Locate and identify every blood parasite.
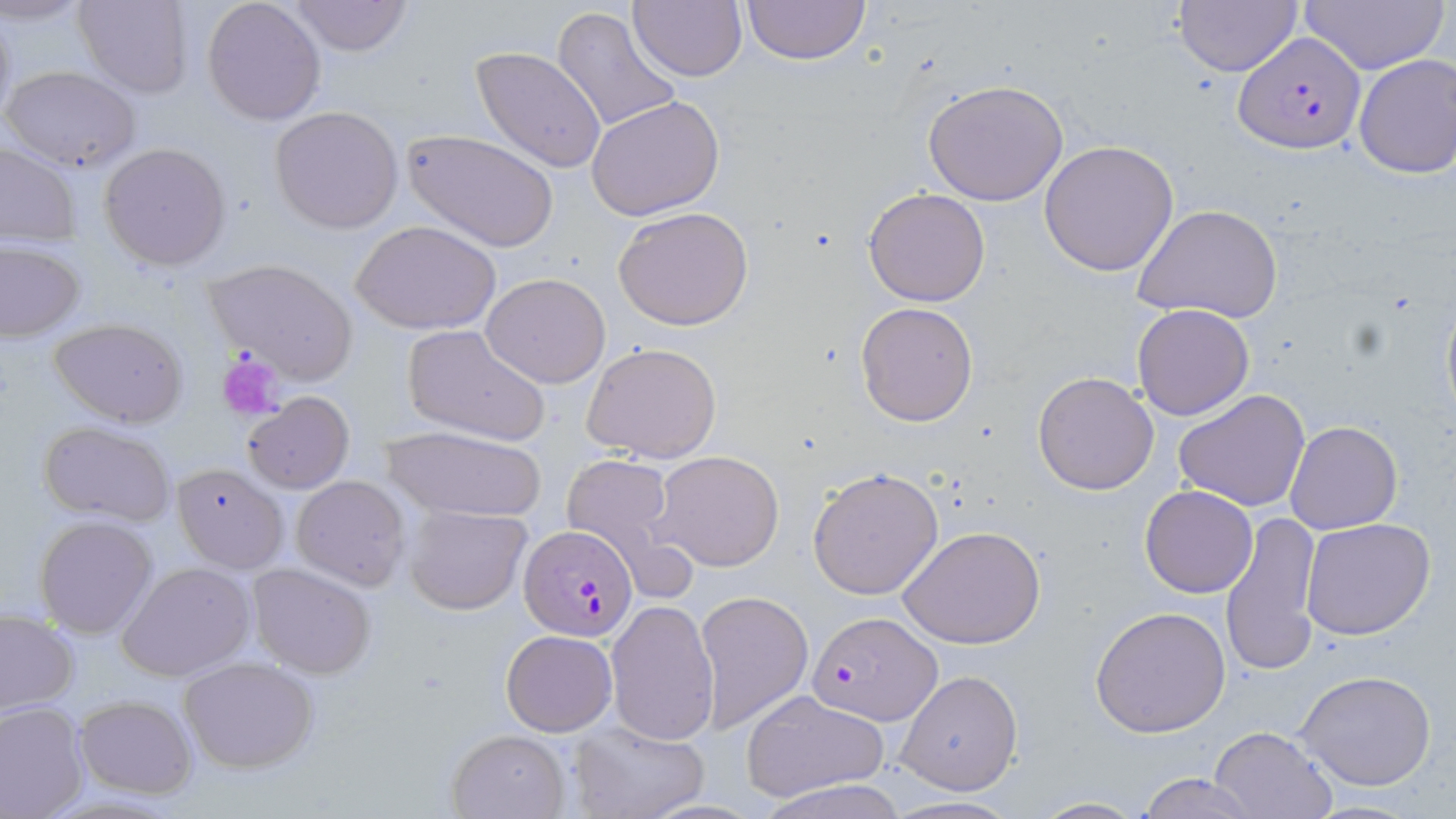

Approximate bounding boxes as [x1, y1, x2, y2] in pixels.
Plasmodium falciparum-infected red blood cells: [1234, 32, 1366, 155], [518, 524, 639, 641], [809, 611, 940, 726].
No Plasmodium ovale, Plasmodium malariae, Plasmodium vivax, Babesia divergens, or Trypanosoma brucei observed.

Summary:
  - Uninfected red blood cell locations: [73, 0, 192, 98], [201, 0, 327, 124], [289, 0, 414, 57], [628, 0, 746, 84], [741, 0, 873, 66], [1296, 0, 1448, 75], [1173, 1, 1303, 75], [0, 2, 18, 129], [551, 5, 683, 136], [471, 45, 607, 173], [1353, 53, 1456, 178], [1, 64, 143, 171], [924, 80, 1068, 208], [587, 95, 725, 221], [270, 106, 403, 232], [402, 127, 560, 254], [1039, 140, 1179, 276], [0, 141, 82, 248], [99, 142, 231, 270], [864, 187, 990, 307], [1136, 203, 1284, 326], [612, 206, 755, 332], [351, 219, 500, 335], [1, 241, 86, 340], [202, 258, 359, 383], [481, 274, 612, 389], [1440, 281, 1456, 429], [856, 302, 978, 426], [1132, 303, 1255, 419], [47, 317, 190, 426], [400, 324, 551, 447], [581, 343, 724, 464], [1032, 370, 1160, 495], [1174, 388, 1313, 513], [242, 391, 355, 494], [36, 421, 179, 527], [1284, 421, 1402, 535], [378, 425, 550, 524], [651, 450, 784, 571], [559, 454, 684, 574], [170, 464, 290, 573], [808, 468, 944, 599], [291, 475, 412, 593], [1139, 484, 1259, 598], [403, 503, 531, 615], [1219, 507, 1322, 679], [34, 516, 159, 638], [1302, 518, 1436, 641], [899, 525, 1046, 648], [117, 562, 257, 682], [247, 563, 378, 678], [694, 590, 813, 734], [605, 600, 721, 746], [1091, 604, 1231, 739], [0, 610, 79, 717], [500, 630, 617, 737], [179, 656, 320, 774], [895, 669, 1023, 794], [1295, 671, 1439, 791], [740, 689, 890, 803], [73, 694, 197, 799], [0, 699, 90, 818], [570, 720, 709, 819], [1207, 726, 1338, 819], [443, 728, 569, 817], [1137, 773, 1259, 819], [755, 777, 911, 817], [1030, 796, 1145, 817], [1304, 798, 1423, 817]
  - Platelet locations: [218, 352, 286, 420]
  - Slide-level diagnosis: Plasmodium falciparum
  - Image size: 1456×819 pixels
  - Modality: optical microscopy
  - Preparation: thin blood smear
  - Stain: May-Grünwald-Giemsa
  - Field of view: single
  - Magnification: 1000x